State which parasite is depicted.
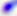

Toxoplasma gondii.

{
  "magnification": "400x",
  "modality": "photomicrograph"
}